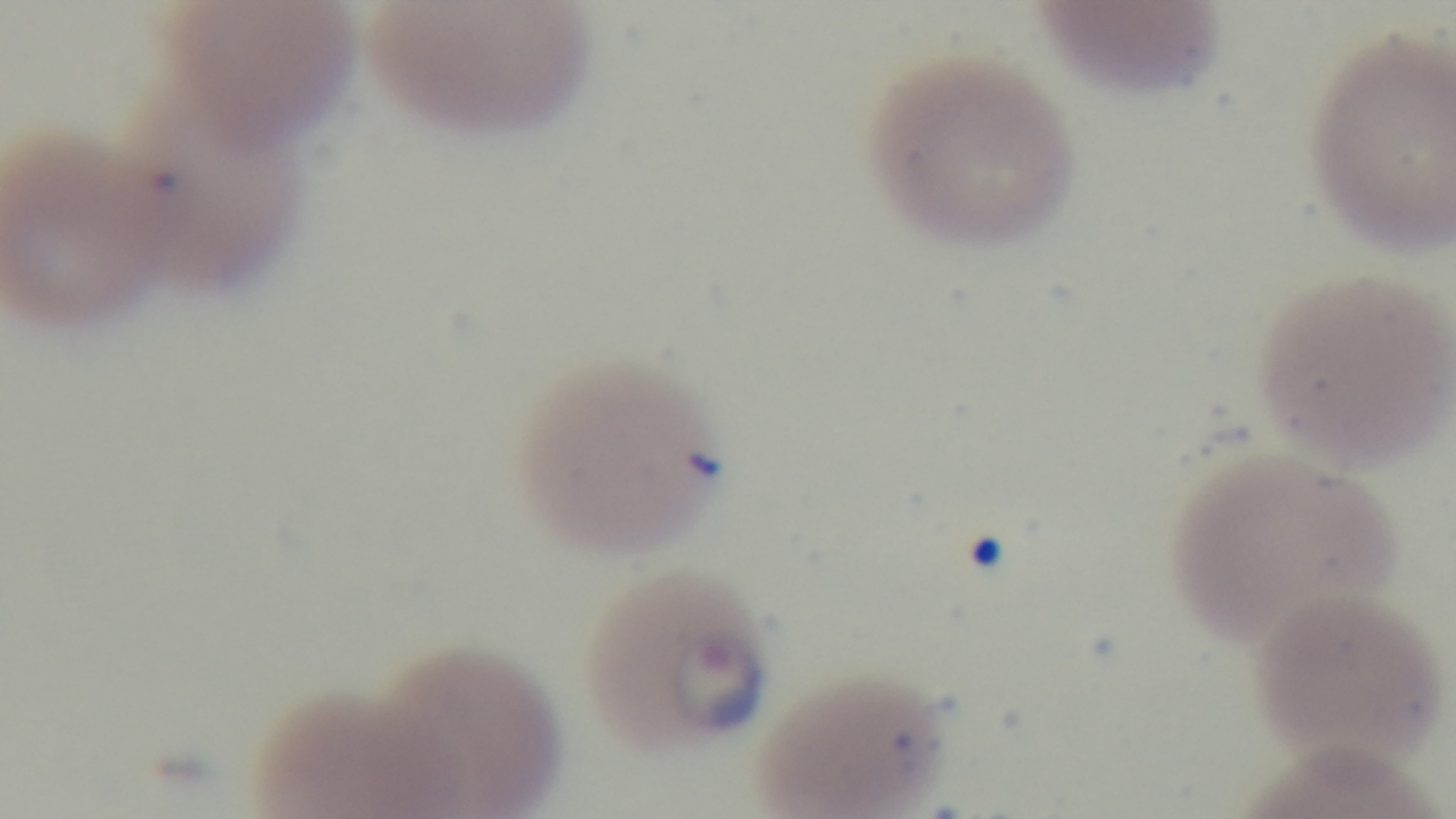
Summary:
  - Preparation: thin smear
  - Stain: Giemsa
  - Modality: light microscopy
  - Objective: 100x oil immersion
  - Capture: mounted 4K digital camera
  - Field of view: one from the slide
  - Malaria status: infected